Assess this cell for malaria.
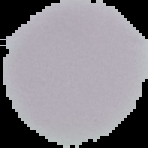

It is uninfected.

Summary:
  - Preparation: thin blood film
  - Image size: 148×148 pixels
  - Image type: segmented cell region with the area outside set to black